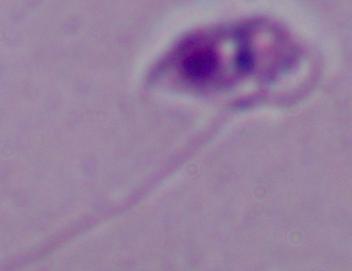 Captured at 1000x magnification. A Leishmania parasite is seen. Photomicrograph.